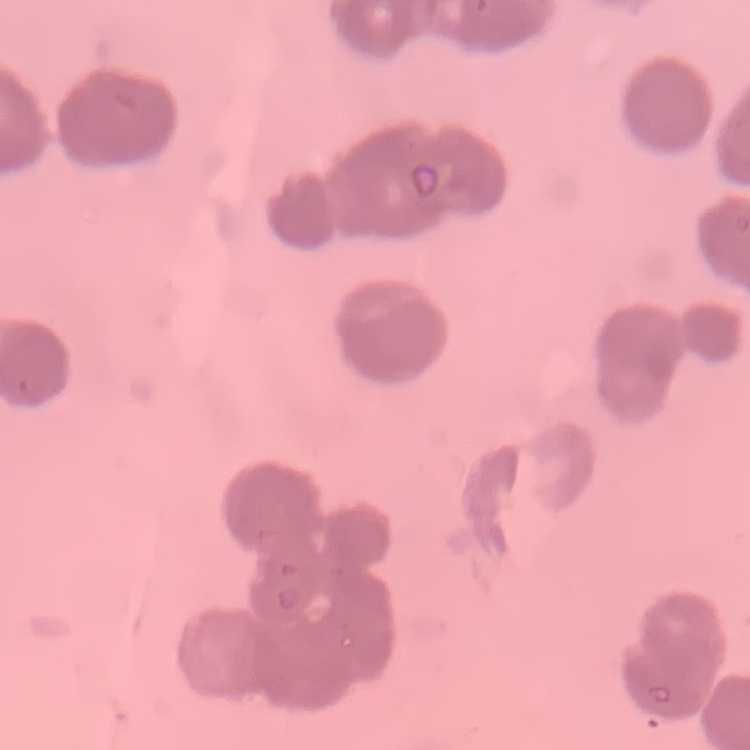

red blood cell morphology = rouleaux formation
stain = Field's or Giemsa
preparation = thin blood film
image type = square crop of a larger photomicrograph